Give a bounding box for every artifact (platelet-like body, stain precipitate, or debris).
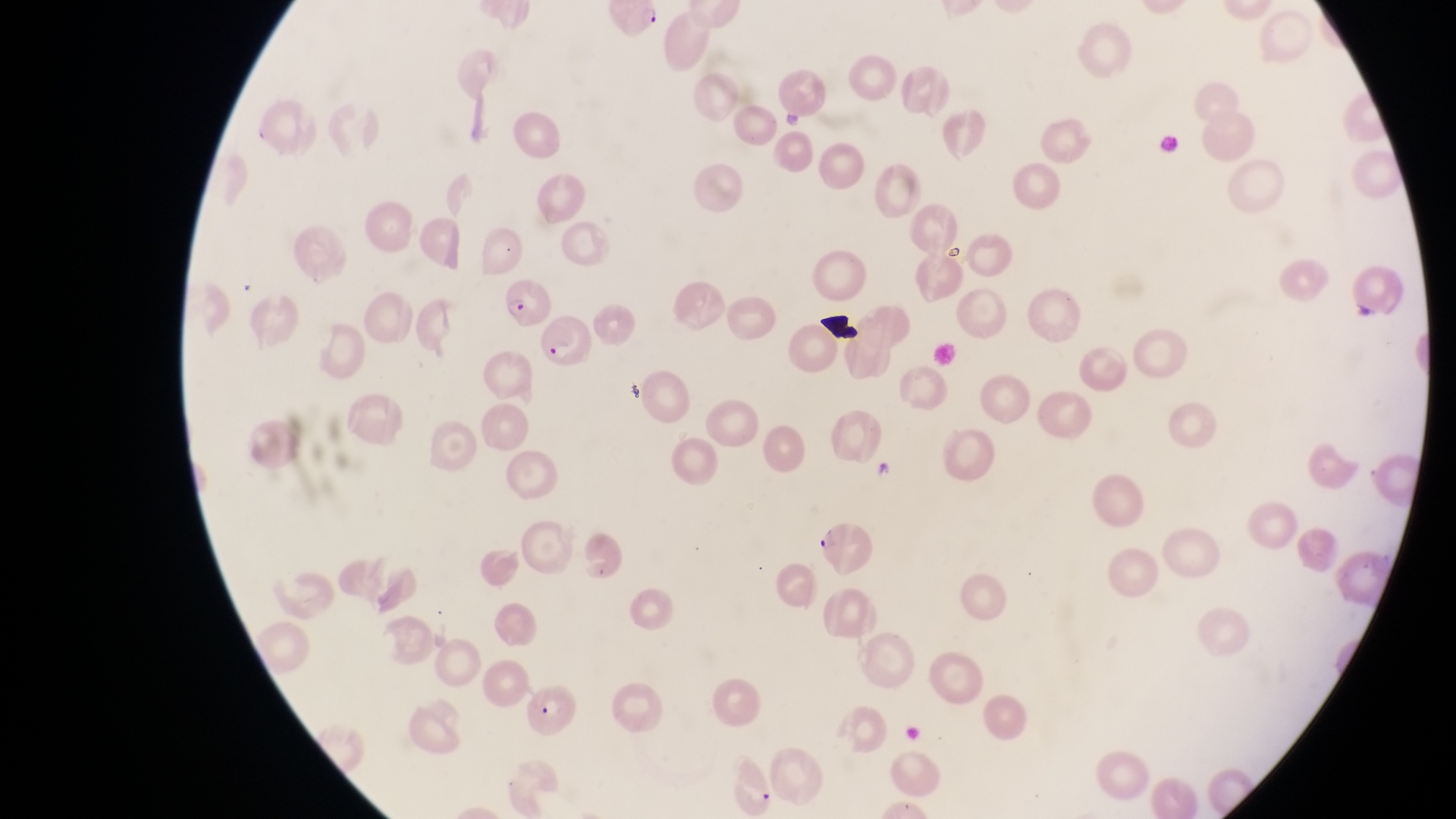
Approximate bounding boxes as left top right bottom in pixels.
Artifacts (platelet-like body, stain precipitate, or debris): 821 310 862 341.

Parasitised red blood cell locations: 608 5 662 41; 502 280 555 327; 547 312 599 368; 817 516 878 573; 515 687 589 743. Sample from Uganda. Image is 1456×819 pixels. Thin blood film. Magnification of 1000x. Photographed through the eyepiece of an Olympus CX-23 microscope with a smartphone camera. One field of view.